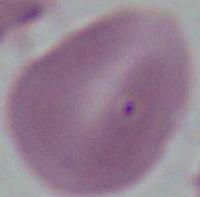 Captured at 1000x magnification. Micrograph. A red blood cell is seen.